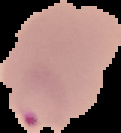
Summary:
  - Image size: 121×133 pixels
  - Preparation: thin blood film
  - Result: Plasmodium parasites detected
  - Image type: segmented cell region with the area outside set to black